Assess this cell for malaria.
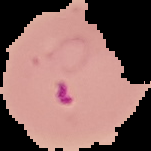

It is parasitized.

Summary:
  - Preparation: thin blood smear
  - Image type: cell region segmented out of the field of view; surrounding area masked to black
  - Image size: 151×151 pixels